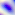
identification = Toxoplasma gondii
modality = micrograph
magnification = 400x